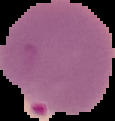

Summary:
  - Image type: cell region segmented out of the field of view; surrounding area masked to black
  - Image size: 115×121 pixels
  - Preparation: thin blood film
  - Malaria status: parasitized